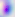
Summary:
  - Identification: Toxoplasma gondii
  - Modality: photomicrograph
  - Magnification: 400x